Describe the morphology of the erythrocytes.
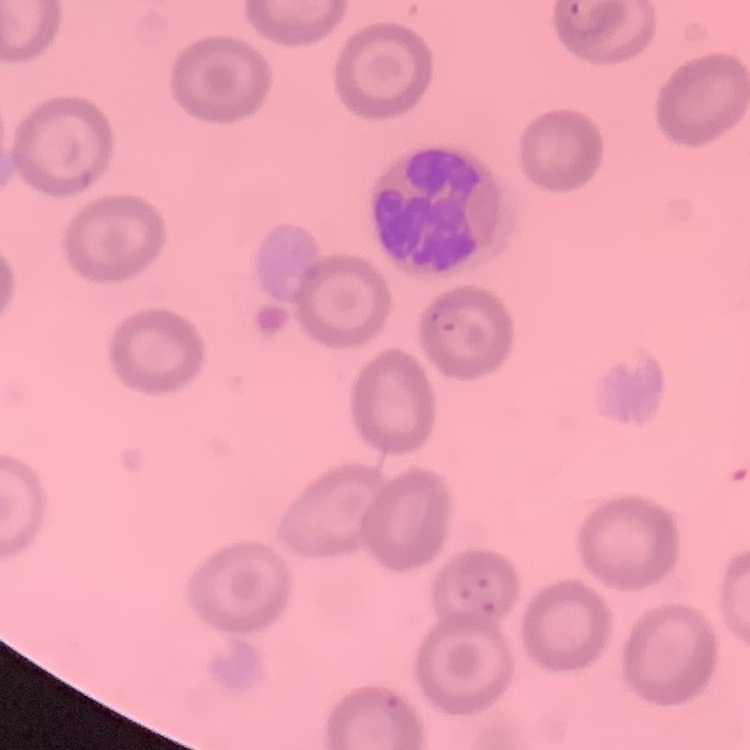

No rouleaux formation.

Field's or Giemsa stain. Square crop of a larger photomicrograph. Thin blood smear.